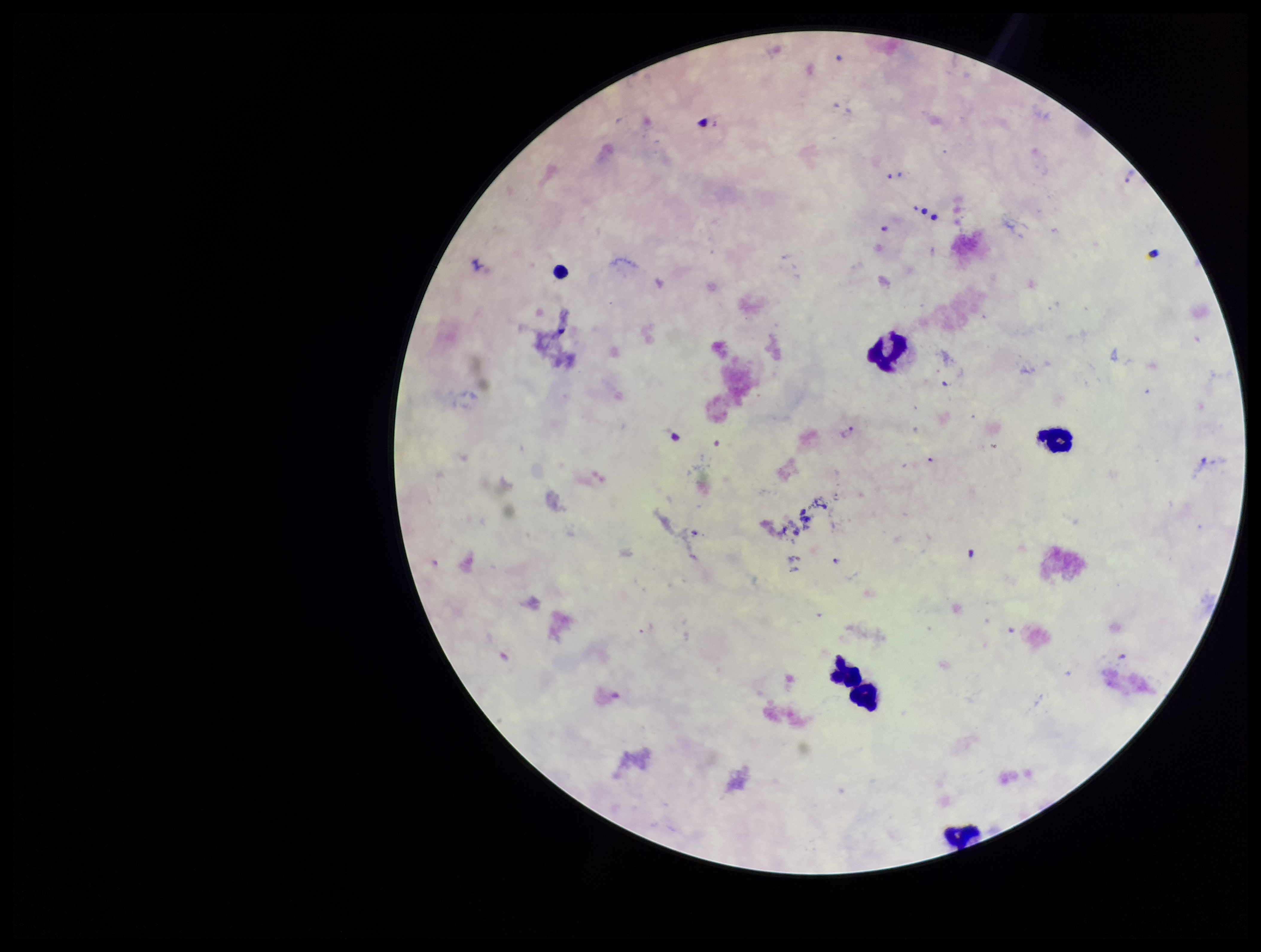
Parasite count: 2. Giemsa stain. Preparation: thick. Photographed through the microscope eyepiece with a smartphone camera. One field from this slide. Patient malaria status: positive. Species reported for this patient: Plasmodium falciparum. Plasmodium parasites: seen. Leukocyte count: 4. Image is 1261×952 pixels.